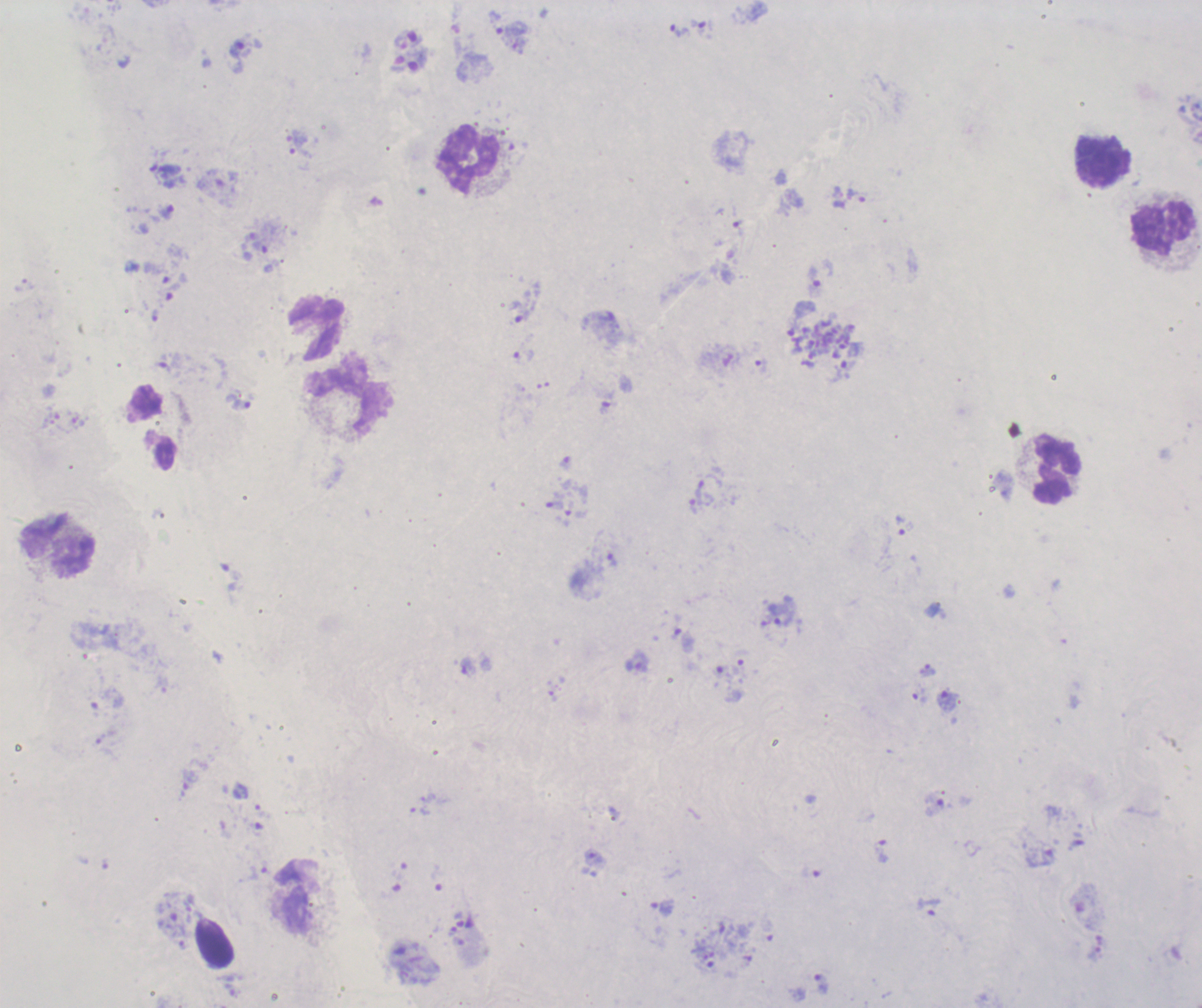

Approximate object centers, in pixels from the top-left corner.
Summary:
  - Schizont locations: (x=820, y=345)
  - Leukocyte locations: (x=469, y=160), (x=1102, y=161), (x=1163, y=227), (x=317, y=328), (x=349, y=397), (x=1057, y=469), (x=58, y=547)
  - Trophozoite locations: (x=699, y=27), (x=680, y=30), (x=511, y=38), (x=245, y=55), (x=850, y=199), (x=166, y=212), (x=814, y=282), (x=521, y=313), (x=760, y=366), (x=609, y=403), (x=241, y=405), (x=555, y=504), (x=900, y=525), (x=611, y=561), (x=784, y=617), (x=637, y=663), (x=468, y=666), (x=927, y=670), (x=947, y=701), (x=935, y=805), (x=881, y=851), (x=596, y=858), (x=1040, y=858), (x=928, y=906), (x=663, y=907), (x=820, y=983)
  - Life-cycle stages observed: trophozoite, schizont
  - Field of view: one from this slide
  - Stain: Romanowsky
  - Magnification: 100x
  - Background quality: poor
  - Context: previously used in an actual diagnosis
  - Result: Plasmodium parasites detected
  - Image size: 1202×1008 pixels
  - Preparation: thick smear of blood